Assess the morphology of the red blood cells.
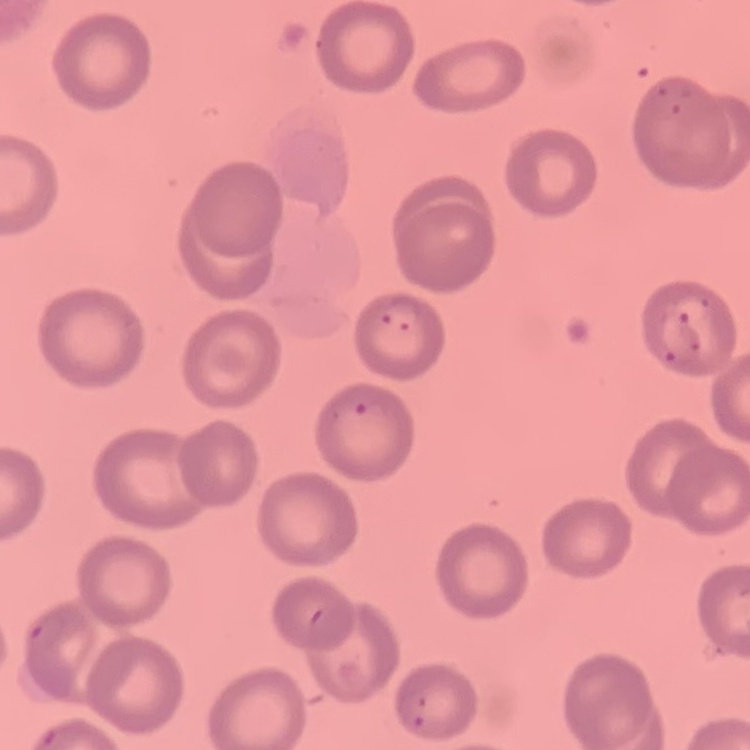

No rouleaux formation.

stain = Field's or Giemsa
image type = one tile cut from a larger photomicrograph
preparation = thin blood smear